Report the malaria status of this cell.
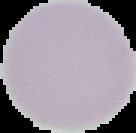
It is uninfected.

image_size: 136×133 pixels
preparation: thin blood film
image_type: cell region segmented out of the field of view; surrounding area masked to black